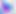
{
  "magnification": "400x",
  "modality": "photomicrograph",
  "identification": "Toxoplasma gondii"
}